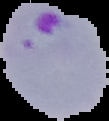

Image is 109×121 pixels. Malaria status: parasitized. The area outside the segmented cell region is set to black. From a thin blood film.